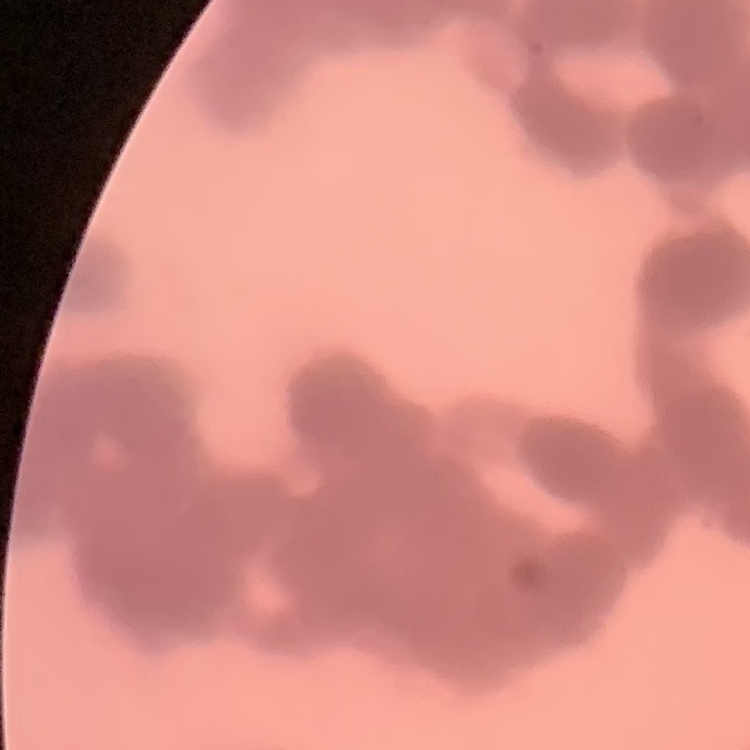
Summary:
  - Erythrocyte morphology: rouleaux formation
  - Stain: Field's or Giemsa
  - Image type: square crop of a larger photomicrograph
  - Preparation: thin blood film